Comment on the morphology of the red blood cells.
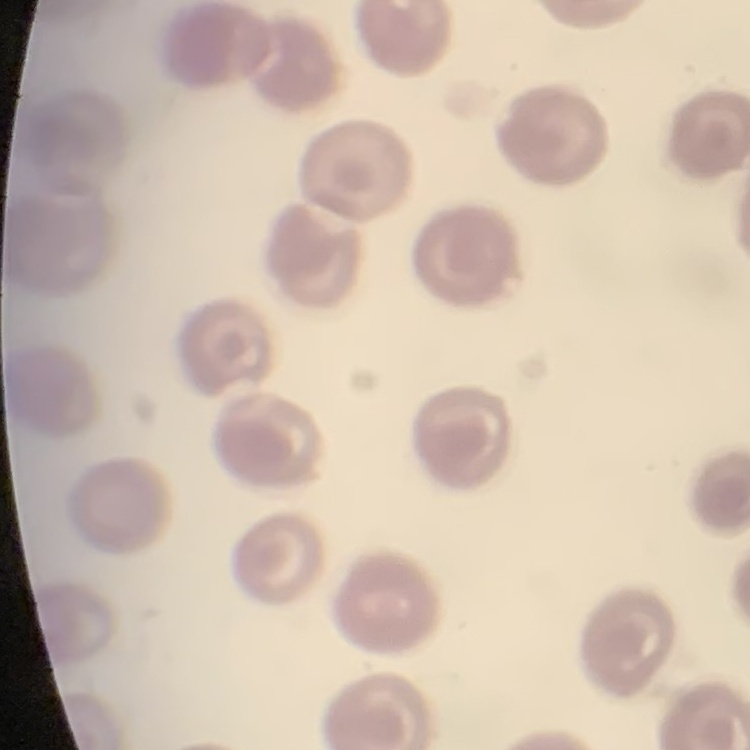
They show no rouleaux formation.

stain = Field's or Giemsa
preparation = thin peripheral smear
image type = one tile cut from a larger photomicrograph